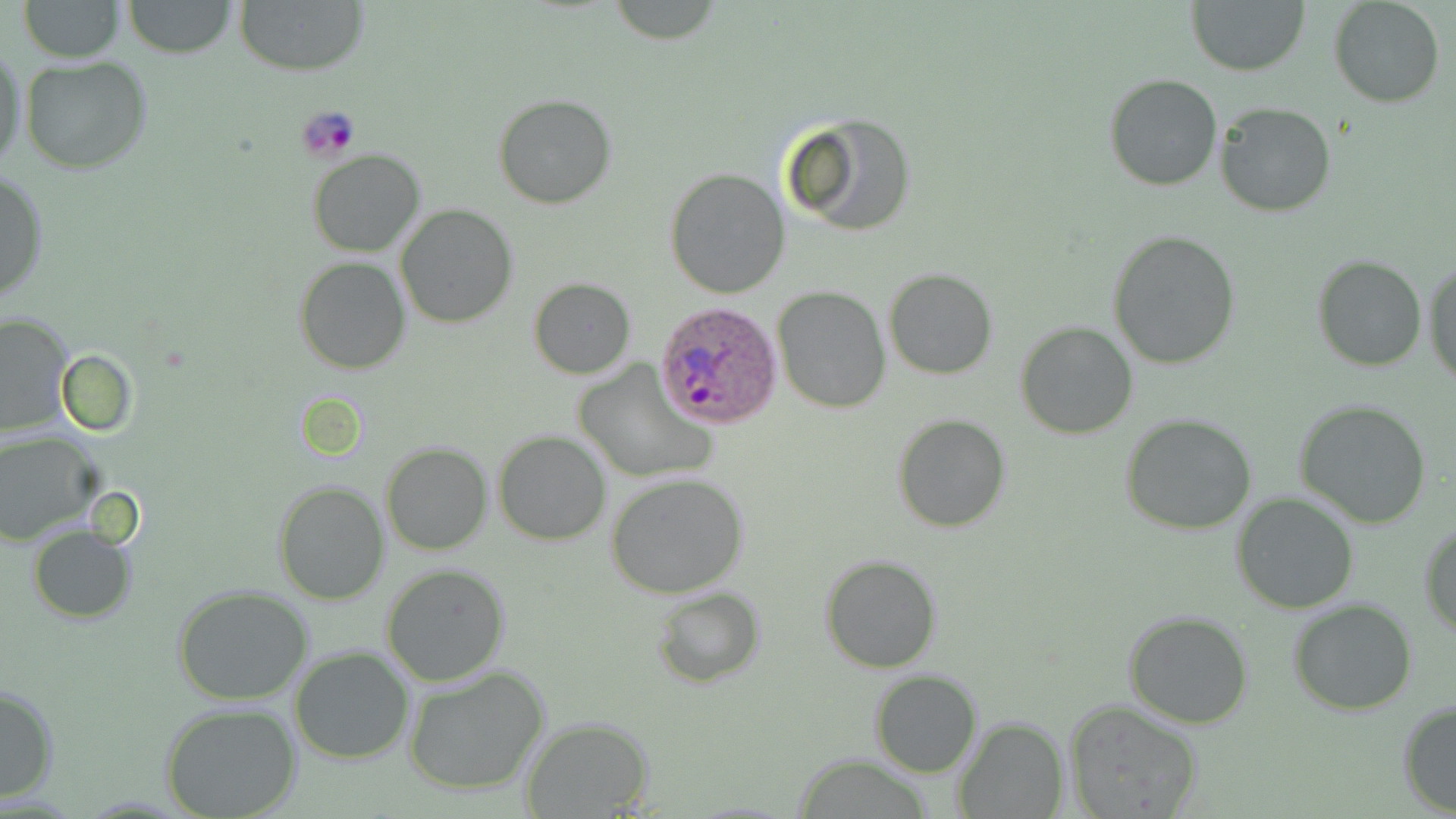
Summary:
  - Coordinate format: approximate bounding boxes as (x1, y1, x2, y2) in pixels
  - Uninfected red blood cell locations: (17, 0, 125, 61), (122, 0, 238, 57), (235, 0, 367, 77), (1187, 0, 1309, 77), (1330, 0, 1444, 107), (0, 41, 27, 179), (19, 56, 154, 173), (1104, 74, 1221, 192), (493, 93, 618, 208), (1215, 101, 1337, 217), (782, 111, 919, 236), (307, 149, 425, 258), (664, 167, 790, 299), (1, 168, 47, 305), (395, 203, 518, 328), (1106, 231, 1243, 371), (1311, 254, 1429, 372), (294, 256, 409, 374), (1422, 256, 1456, 390), (884, 269, 997, 379), (529, 278, 635, 378), (773, 288, 891, 412), (0, 314, 74, 436), (1016, 320, 1140, 440), (56, 350, 136, 435), (573, 360, 715, 484), (1294, 398, 1433, 529), (1119, 413, 1258, 535), (893, 414, 1010, 532), (493, 430, 611, 545), (0, 432, 100, 544), (380, 442, 492, 555), (606, 471, 749, 597), (273, 480, 388, 604), (1231, 493, 1359, 614), (1418, 518, 1456, 636), (27, 527, 135, 623), (820, 554, 942, 673), (381, 561, 512, 685), (172, 585, 313, 706), (652, 587, 764, 689), (1289, 598, 1418, 714), (1123, 610, 1254, 730), (289, 646, 415, 765), (403, 664, 550, 796), (870, 671, 982, 777), (0, 685, 60, 802), (1061, 698, 1206, 819), (1397, 700, 1456, 816), (160, 702, 302, 819), (520, 716, 654, 816), (952, 716, 1070, 819), (790, 757, 941, 817)
  - Plasmodium ovale-infected red blood cell locations: (655, 300, 783, 429)
  - Slide-level diagnosis: Plasmodium ovale
  - Preparation: thin blood smear
  - Modality: light microscopy
  - Field of view: one of a larger specimen
  - Magnification: 1000x
  - Stain: May-Grünwald-Giemsa
  - Image size: 1456×819 pixels